Report the malaria status of this cell.
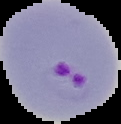

Parasitized.

image type = segmented cell region on a black background
image size = 121×124 pixels
preparation = thin blood film